Report the malaria status of this cell.
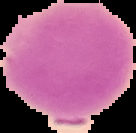

It is uninfected.

Image is 136×133 pixels. The area outside the segmented cell region is set to black. From a thin blood smear.